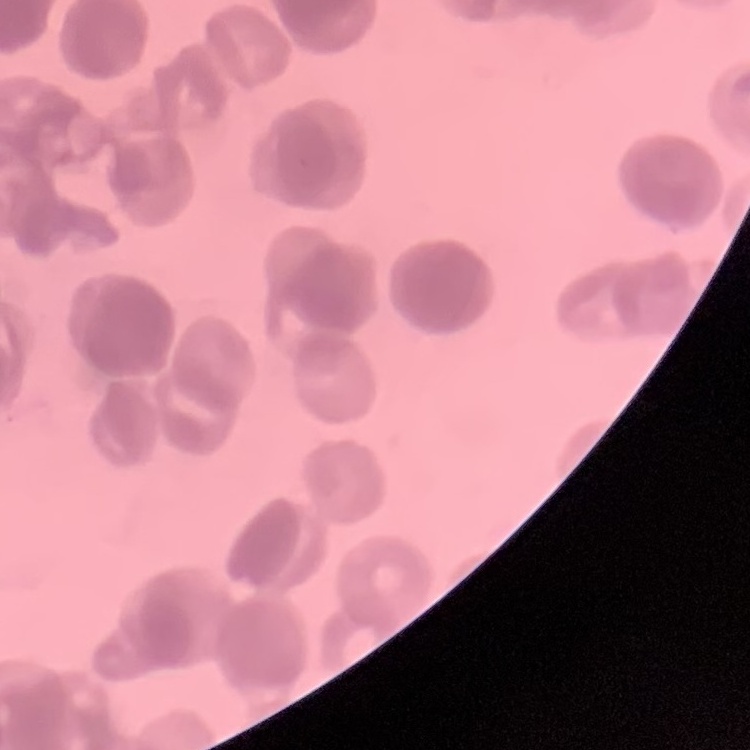

Summary:
  - Erythrocyte morphology: rouleaux formation
  - Preparation: thin blood smear
  - Image type: one tile cut from a larger photomicrograph
  - Stain: Field's or Giemsa